Assess this cell for malaria.
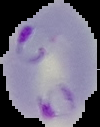
Parasitized.

From a thin blood film. Image is 100×127 pixels. Segmented cell region on a black background.